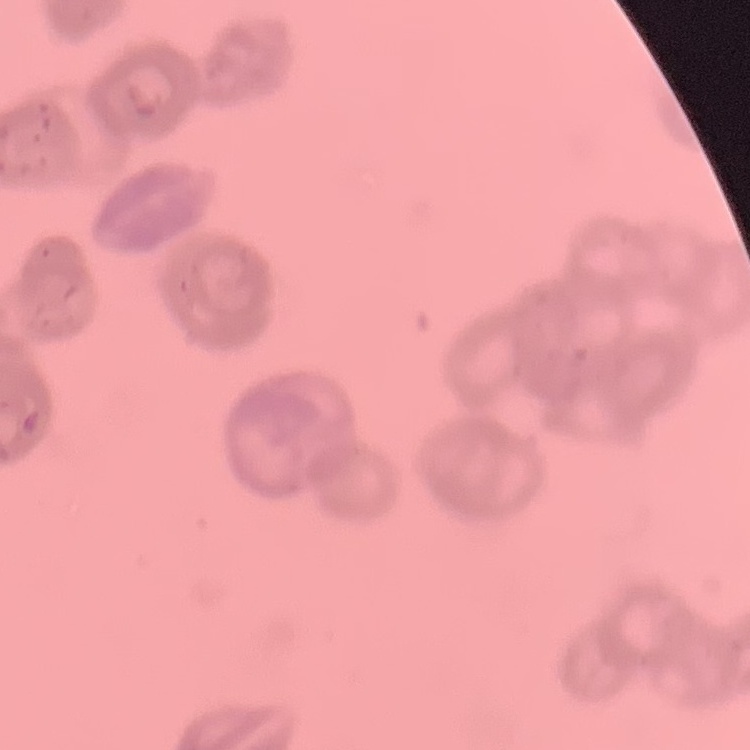
Summary:
  - Red blood cell morphology: rouleaux formation
  - Image type: square crop of a larger photomicrograph
  - Stain: Field's or Giemsa
  - Preparation: thin blood film